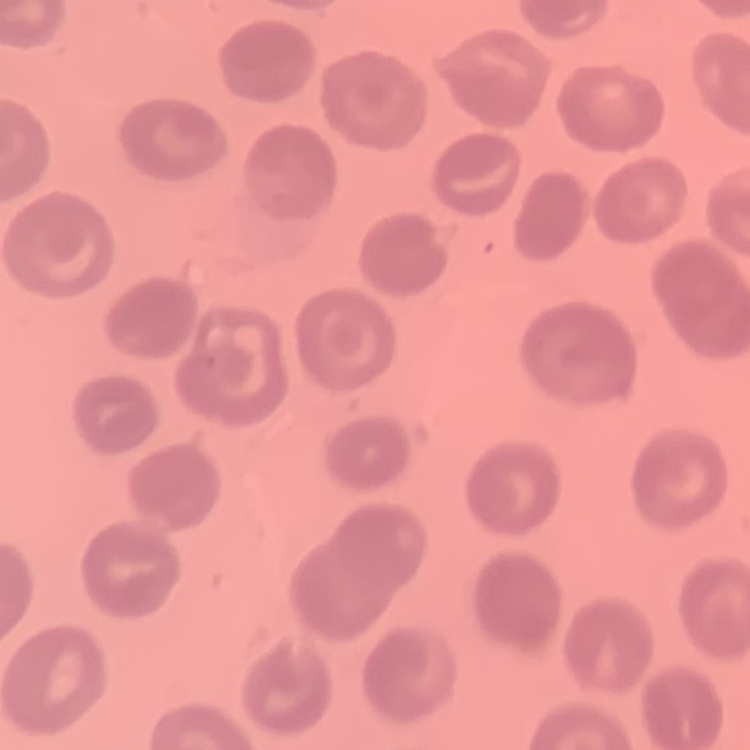

erythrocyte_morphology: no rouleaux formation
preparation: thin peripheral smear
stain: Field's or Giemsa
image_type: one tile cut from a larger photomicrograph